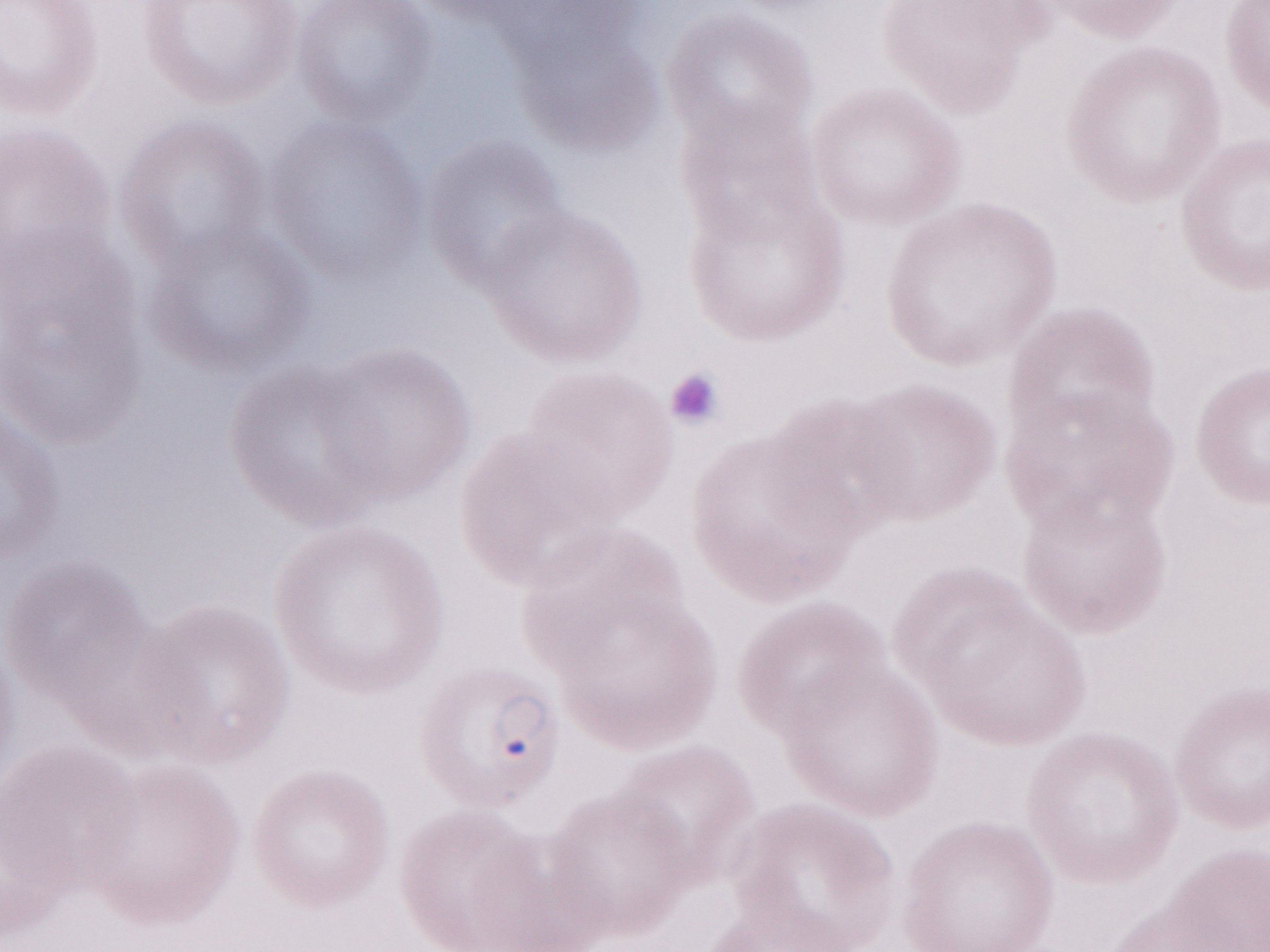 Image is 1270×952 pixels. Single field of view. Malaria diagnosis (patient-level): positive. Magnification: 1,000x. May-Grünwald-Giemsa stain. Olympus BX43 microscope, Olympus DP73 camera. Thin blood film.